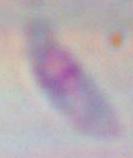

modality = micrograph
identification = Toxoplasma gondii
magnification = 1000x